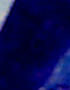
{
  "magnification": "1000x",
  "identification": "white blood cell",
  "modality": "photomicrograph"
}